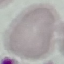
Summary:
  - Malaria status: uninfected
  - Image type: automatically extracted cell patch, resized to 64 × 64 pixels
  - Stain: Giemsa
  - Preparation: thin blood smear
  - Capture: smartphone camera at the microscope eyepiece